Locate every malaria parasite.
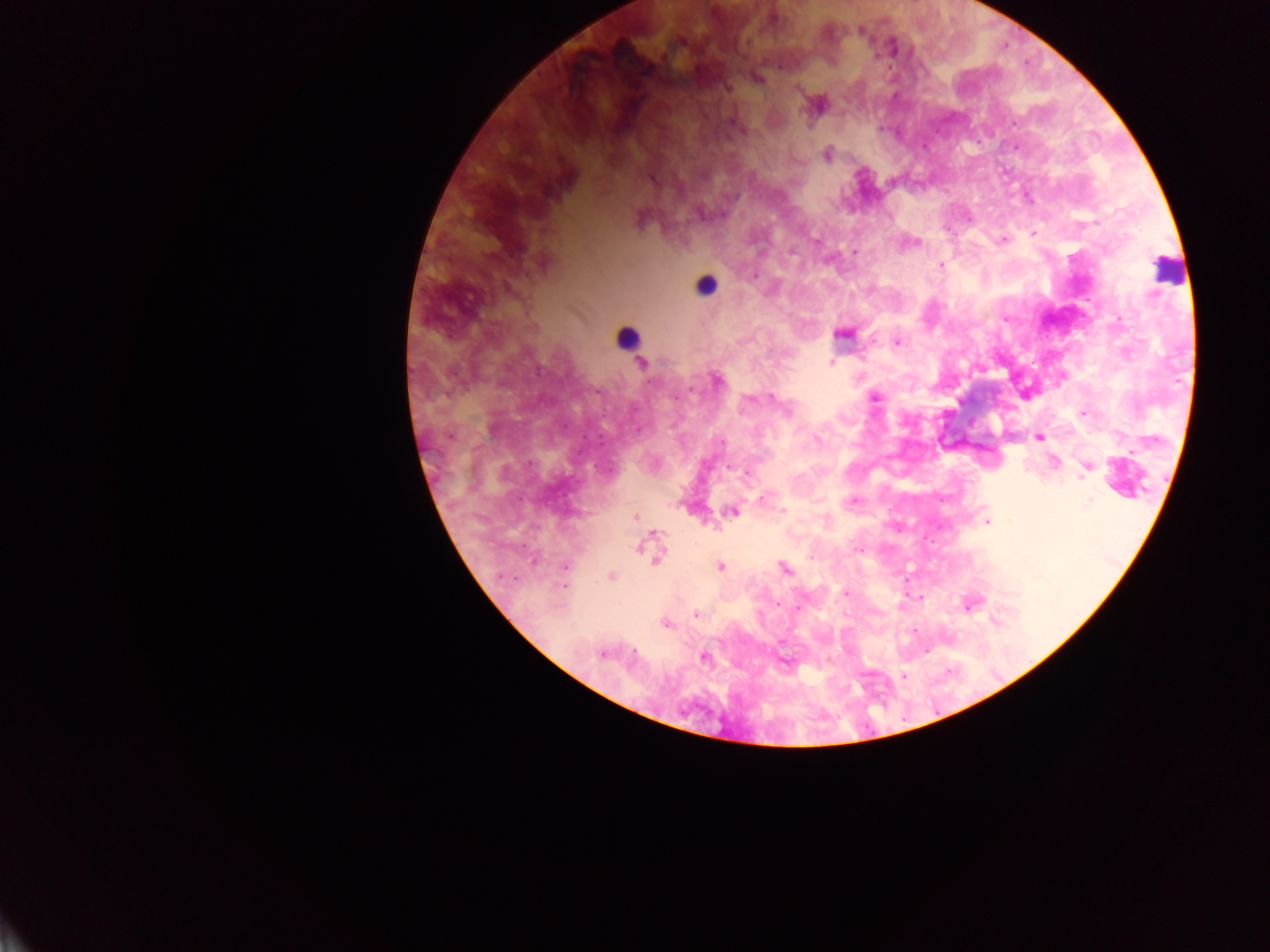

Approximate centers as x y in pixels.
Malaria parasites: 861 30; 758 79; 728 88; 798 89; 731 122; 1013 123; 827 155; 652 179; 722 214; 639 220; 1033 233; 816 239; 1002 240; 917 242; 791 252; 854 252; 940 265; 754 276; 509 289; 842 334; 897 342; 831 362; 642 363; 718 380; 875 397; 772 398; 750 399; 786 409; 1082 413; 1039 437; 722 443; 1054 461; 730 467; 1086 469; 747 472; 1083 478; 761 499; 854 501; 1088 505; 783 510; 732 511; 635 516; 987 522; 655 533; 638 548; 857 549; 810 557; 656 558; 719 566; 565 567; 784 568; 612 576; 564 586; 845 594; 778 605; 970 605; 799 606; 696 613; 996 620; 666 624; 633 652; 601 654; 704 657; 903 676.

Leukocyte locations: 1167 271; 706 285; 627 338. Image is 1270×952 pixels. Collected in Ghana. Thick blood smear. Photographed through a microscope with a mobile-phone camera. One field of view.